Locate every blood parasite and identify its species.
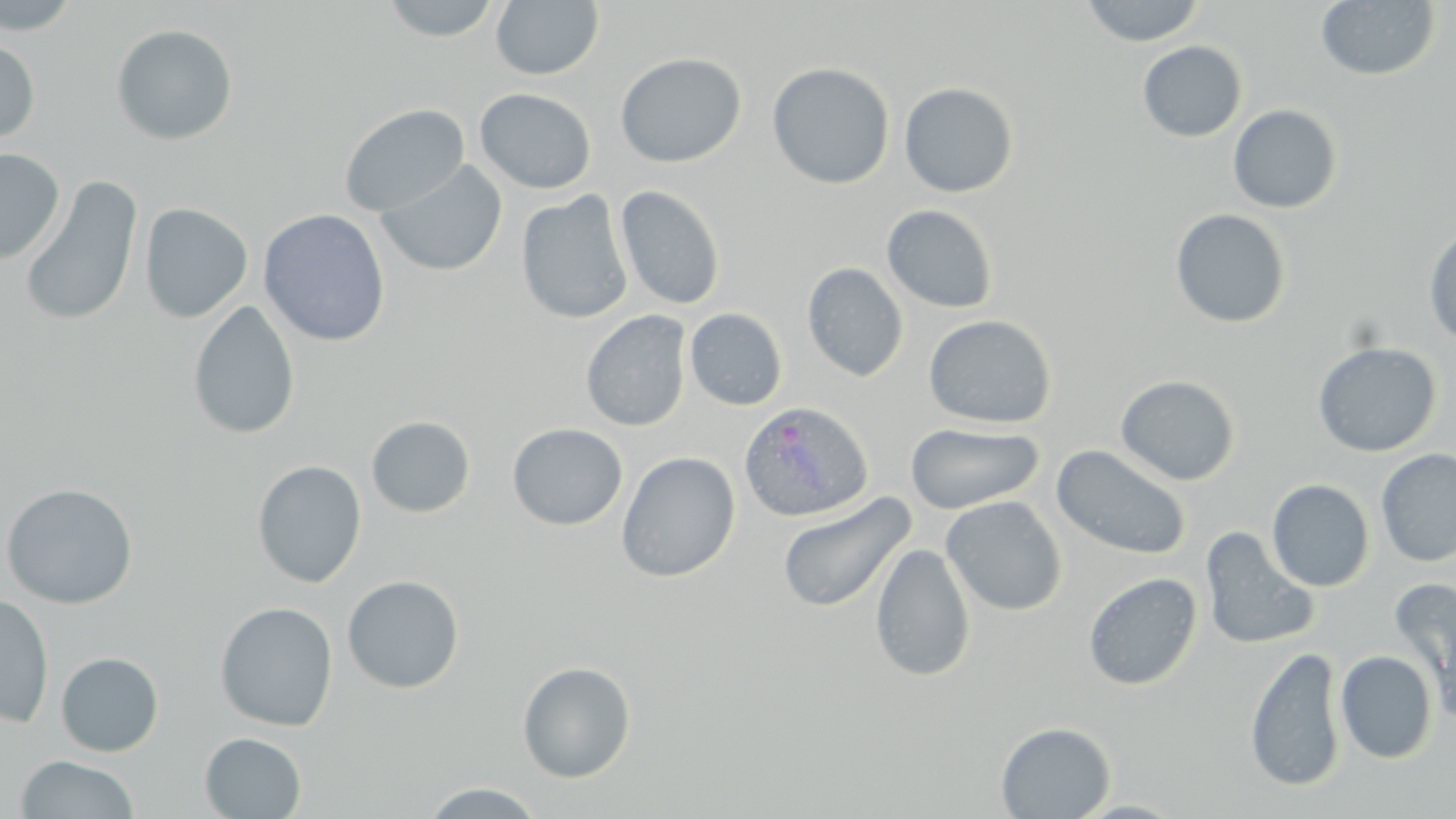
Approximate bounding boxes as (x1, y1, x2, y2) in pixels.
Plasmodium ovale-infected red blood cells: (738, 401, 873, 523).
No Plasmodium falciparum, Plasmodium malariae, Plasmodium vivax, Babesia divergens, or Trypanosoma brucei observed.

{
  "slide_level_diagnosis": "Plasmodium ovale",
  "magnification": "1000x",
  "field_of_view": "single",
  "uninfected_red_blood_cell_locations": "approximate bounding boxes as (x1, y1, x2, y2) in pixels: (0, 0, 83, 35), (379, 0, 503, 41), (1080, 0, 1205, 46), (490, 1, 604, 80), (1315, 1, 1441, 81), (111, 23, 239, 146), (0, 36, 40, 145), (1137, 41, 1247, 143), (615, 52, 746, 168), (767, 62, 895, 190), (899, 81, 1019, 197), (475, 88, 597, 194), (338, 103, 470, 217), (1228, 104, 1343, 214), (0, 148, 65, 264), (374, 159, 509, 278), (19, 175, 143, 328), (614, 185, 726, 311), (515, 191, 634, 325), (139, 202, 253, 323), (881, 204, 999, 314), (1170, 208, 1292, 329), (258, 209, 391, 347), (1423, 222, 1456, 348), (802, 262, 908, 383), (187, 300, 301, 440), (684, 308, 787, 411), (580, 310, 692, 432), (923, 314, 1056, 429), (1312, 341, 1442, 458), (1115, 374, 1241, 486), (366, 416, 476, 517), (507, 423, 627, 530), (905, 423, 1044, 514), (1051, 444, 1191, 560), (1376, 448, 1456, 567), (616, 451, 740, 583), (252, 459, 367, 588), (1267, 479, 1375, 592), (0, 482, 138, 609), (777, 491, 916, 614), (940, 496, 1067, 615), (1199, 526, 1320, 652), (870, 542, 976, 683), (1083, 572, 1202, 690), (341, 575, 465, 694), (1390, 576, 1456, 704), (0, 593, 55, 728), (214, 601, 338, 731), (1245, 646, 1347, 793), (1335, 650, 1438, 764), (55, 652, 164, 756), (517, 660, 637, 783), (995, 721, 1116, 818), (199, 732, 307, 819), (15, 754, 141, 818), (420, 781, 548, 818)",
  "image_size": "1456×819 pixels",
  "modality": "light microscopy",
  "stain": "May-Grünwald-Giemsa",
  "preparation": "thin blood smear"
}